Locate and identify every blood parasite.
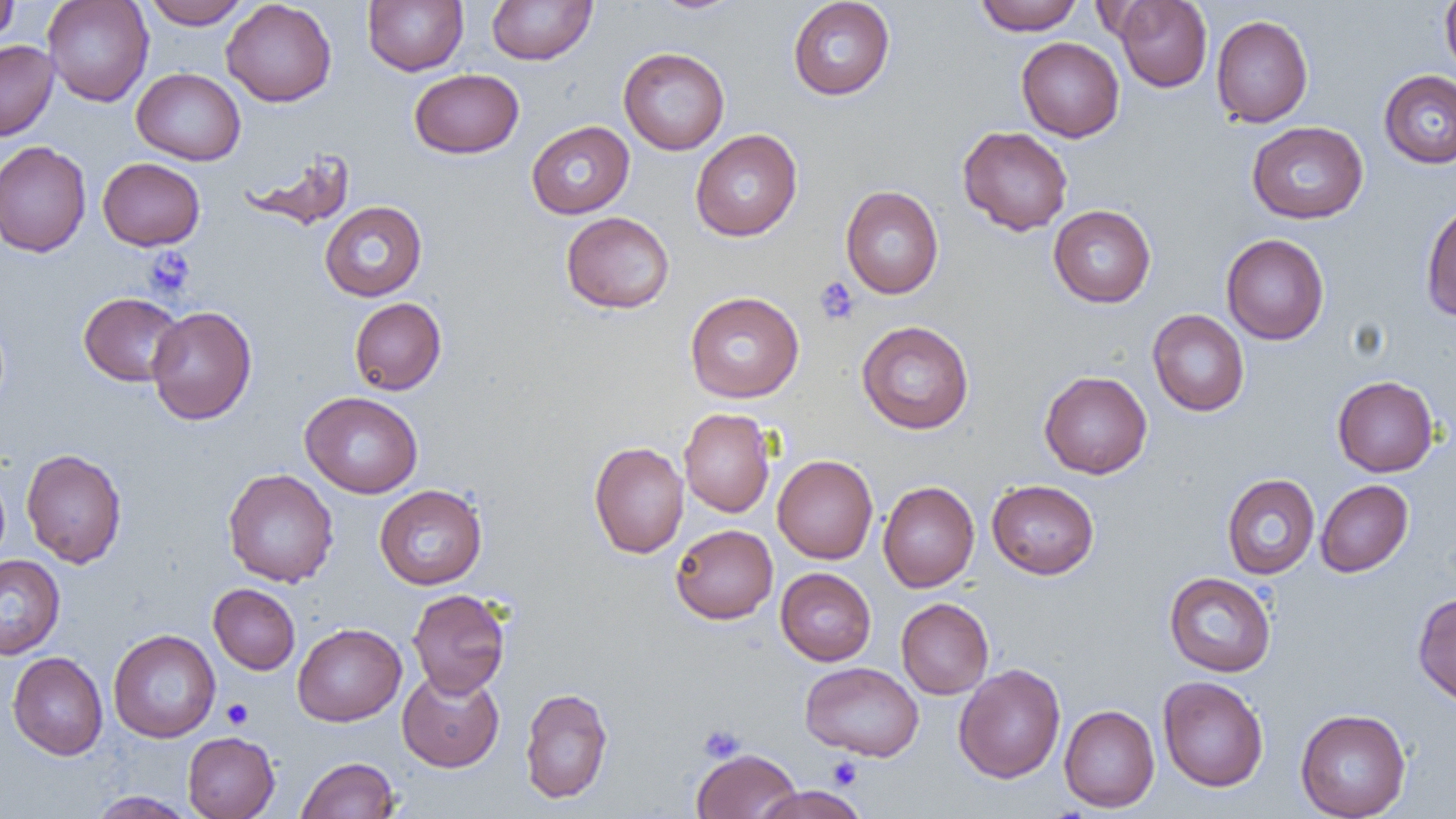
No blood parasites seen.

Summary:
  - Coordinate format: approximate bounding boxes as [x1, y1, x2, y2] in pixels
  - Platelet locations: [144, 248, 196, 298], [814, 276, 860, 325], [222, 699, 254, 729], [698, 724, 744, 762], [827, 757, 862, 790]
  - Uninfected red blood cell locations: [0, 0, 19, 46], [42, 0, 154, 106], [144, 0, 251, 29], [363, 0, 468, 75], [486, 0, 596, 65], [650, 0, 744, 15], [788, 0, 895, 100], [974, 0, 1084, 35], [1113, 0, 1212, 92], [1440, 0, 1456, 80], [222, 1, 337, 107], [1211, 14, 1313, 127], [1016, 37, 1125, 142], [0, 41, 58, 140], [618, 47, 730, 154], [131, 68, 246, 165], [409, 69, 524, 159], [1378, 70, 1456, 168], [526, 120, 635, 219], [1246, 121, 1369, 224], [957, 126, 1073, 235], [690, 129, 802, 241], [0, 140, 91, 257], [240, 149, 357, 232], [97, 157, 205, 250], [840, 186, 944, 299], [1421, 199, 1456, 323], [319, 201, 427, 301], [1048, 205, 1156, 308], [561, 212, 675, 314], [1221, 233, 1329, 345], [684, 291, 804, 403], [78, 292, 185, 386], [349, 297, 446, 395], [146, 306, 257, 425], [1147, 309, 1249, 416], [856, 320, 974, 434], [1039, 370, 1152, 479], [1332, 375, 1439, 477], [300, 391, 423, 498], [679, 408, 775, 517], [589, 441, 689, 558], [21, 448, 127, 568], [772, 455, 878, 563], [0, 466, 10, 569], [223, 468, 339, 587], [1221, 473, 1320, 579], [986, 479, 1100, 579], [1315, 479, 1414, 577], [878, 481, 979, 592], [374, 484, 487, 589], [670, 524, 778, 624], [0, 554, 65, 660], [776, 567, 876, 665], [1164, 571, 1276, 677], [208, 583, 300, 674], [407, 588, 511, 697], [1412, 591, 1456, 708], [896, 598, 993, 699], [292, 623, 406, 726], [108, 629, 220, 742], [7, 651, 108, 760], [800, 662, 924, 760], [953, 663, 1066, 783], [397, 668, 504, 772], [1157, 675, 1269, 792], [520, 686, 613, 805], [1059, 705, 1159, 812], [1295, 708, 1411, 819], [183, 731, 280, 819], [692, 748, 802, 819], [296, 756, 400, 819], [751, 786, 870, 819], [88, 791, 197, 818]
  - Slide-level diagnosis: no evidence of blood parasites
  - Field of view: single
  - Image size: 1456×819 pixels
  - Modality: optical microscopy
  - Magnification: 1000x
  - Preparation: thin blood film